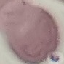
{
  "result": "no malaria parasites seen",
  "preparation": "thin smear",
  "image_type": "cell patch, automatically extracted from a larger field of view and resized to 64 × 64 pixels",
  "capture": "smartphone through the microscope eyepiece",
  "stain": "Giemsa"
}